Assess this cell for malaria.
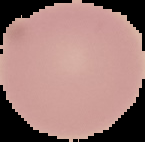
It is uninfected.

From a thin blood smear. Image is 145×142 pixels. The area outside the segmented cell region is set to black.